Locate every Plasmodium falciparum-infected red blood cell.
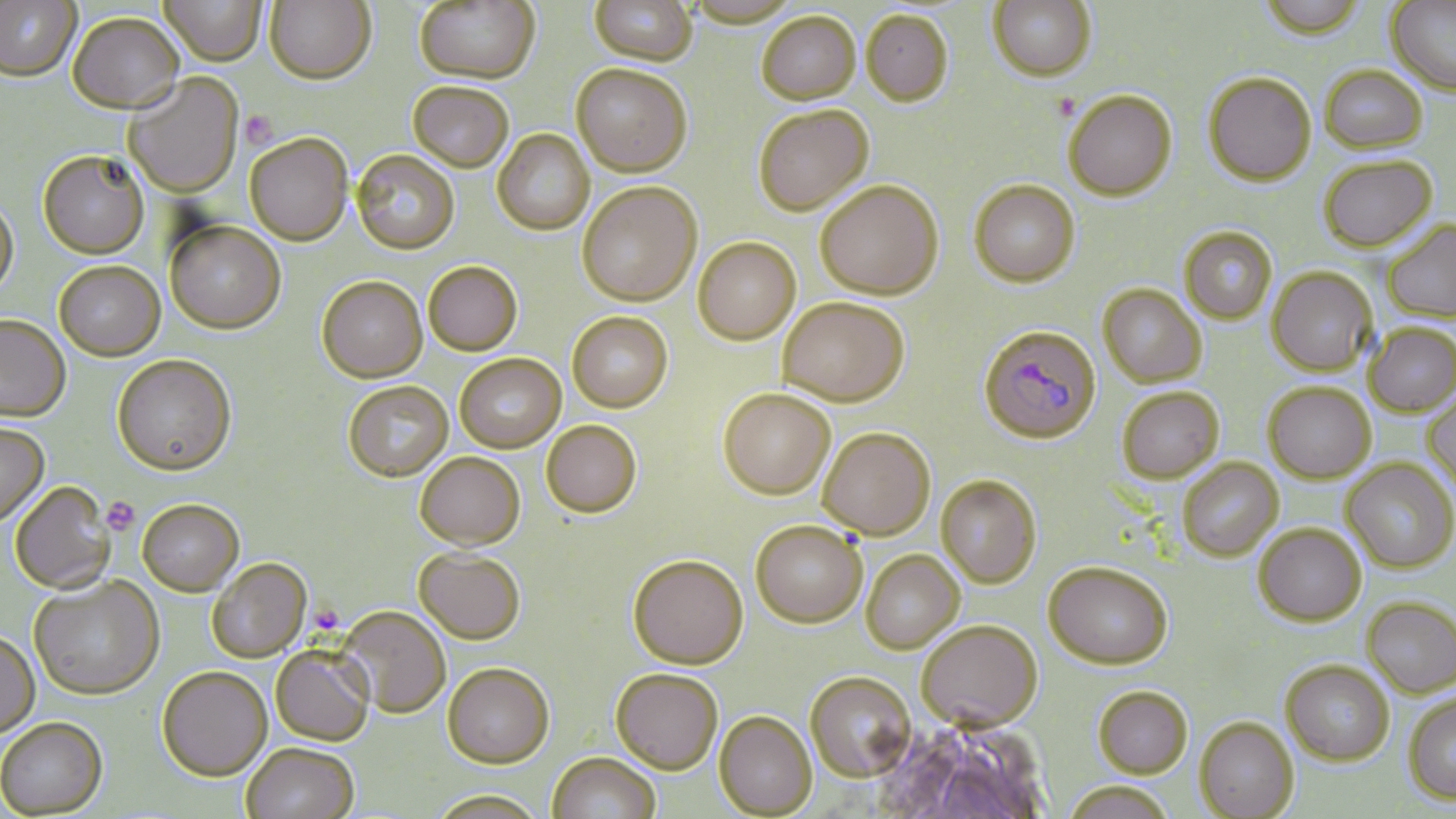
Approximate bounding boxes as named x1/y1/x2/y2 corners in pixels.
Plasmodium falciparum-infected red blood cells: (x1=979, y1=324, x2=1102, y2=444).

Summary:
  - Uninfected red blood cell locations: (x1=159, y1=0, x2=267, y2=66), (x1=265, y1=0, x2=376, y2=84), (x1=988, y1=0, x2=1096, y2=81), (x1=1256, y1=0, x2=1368, y2=41), (x1=0, y1=1, x2=81, y2=80), (x1=413, y1=1, x2=540, y2=83), (x1=590, y1=1, x2=698, y2=66), (x1=683, y1=1, x2=801, y2=28), (x1=1386, y1=1, x2=1456, y2=96), (x1=861, y1=9, x2=953, y2=106), (x1=67, y1=11, x2=184, y2=113), (x1=756, y1=11, x2=861, y2=104), (x1=571, y1=64, x2=692, y2=177), (x1=1320, y1=64, x2=1427, y2=153), (x1=1204, y1=71, x2=1316, y2=186), (x1=123, y1=72, x2=244, y2=198), (x1=408, y1=81, x2=514, y2=172), (x1=1063, y1=89, x2=1176, y2=200), (x1=752, y1=104, x2=874, y2=216), (x1=492, y1=129, x2=595, y2=235), (x1=245, y1=132, x2=353, y2=245), (x1=351, y1=149, x2=460, y2=254), (x1=38, y1=150, x2=149, y2=259), (x1=1319, y1=155, x2=1438, y2=252), (x1=969, y1=179, x2=1080, y2=286), (x1=815, y1=180, x2=943, y2=299), (x1=578, y1=182, x2=702, y2=306), (x1=0, y1=198, x2=19, y2=299), (x1=165, y1=220, x2=286, y2=334), (x1=1383, y1=220, x2=1456, y2=322), (x1=1179, y1=226, x2=1277, y2=324), (x1=693, y1=237, x2=801, y2=344), (x1=424, y1=260, x2=523, y2=355), (x1=54, y1=261, x2=165, y2=361), (x1=1267, y1=267, x2=1377, y2=377), (x1=317, y1=275, x2=427, y2=382), (x1=1098, y1=283, x2=1207, y2=387), (x1=778, y1=296, x2=909, y2=406), (x1=567, y1=311, x2=673, y2=412), (x1=0, y1=315, x2=71, y2=421), (x1=1364, y1=322, x2=1455, y2=417), (x1=455, y1=353, x2=566, y2=452), (x1=112, y1=354, x2=237, y2=476), (x1=343, y1=380, x2=453, y2=481), (x1=1263, y1=382, x2=1376, y2=484), (x1=1117, y1=386, x2=1224, y2=483), (x1=718, y1=388, x2=836, y2=499), (x1=1422, y1=388, x2=1456, y2=495), (x1=541, y1=419, x2=642, y2=517), (x1=0, y1=423, x2=49, y2=526), (x1=818, y1=427, x2=936, y2=540), (x1=415, y1=452, x2=525, y2=549), (x1=1178, y1=457, x2=1283, y2=561), (x1=1342, y1=458, x2=1456, y2=573), (x1=936, y1=474, x2=1042, y2=588), (x1=8, y1=482, x2=116, y2=595), (x1=137, y1=498, x2=244, y2=596), (x1=750, y1=520, x2=867, y2=627), (x1=1254, y1=523, x2=1366, y2=625), (x1=414, y1=547, x2=526, y2=643), (x1=861, y1=549, x2=964, y2=653), (x1=627, y1=554, x2=748, y2=669), (x1=207, y1=558, x2=311, y2=662), (x1=1043, y1=561, x2=1172, y2=669), (x1=29, y1=575, x2=165, y2=700), (x1=1362, y1=596, x2=1456, y2=697), (x1=339, y1=606, x2=451, y2=719), (x1=915, y1=619, x2=1042, y2=731), (x1=0, y1=631, x2=40, y2=738), (x1=270, y1=646, x2=375, y2=746), (x1=1281, y1=659, x2=1394, y2=765), (x1=443, y1=662, x2=554, y2=767), (x1=156, y1=665, x2=272, y2=780), (x1=610, y1=668, x2=723, y2=774), (x1=805, y1=671, x2=916, y2=780), (x1=1093, y1=685, x2=1193, y2=777), (x1=1402, y1=692, x2=1456, y2=804), (x1=715, y1=710, x2=817, y2=817), (x1=1194, y1=716, x2=1299, y2=818), (x1=0, y1=718, x2=108, y2=818), (x1=240, y1=743, x2=359, y2=819), (x1=546, y1=752, x2=661, y2=819), (x1=1062, y1=780, x2=1177, y2=819), (x1=425, y1=789, x2=550, y2=818)
  - Platelet locations: (x1=240, y1=111, x2=278, y2=148), (x1=101, y1=496, x2=141, y2=535)
  - Slide-level diagnosis: Plasmodium falciparum
  - Stain: May-Grünwald-Giemsa
  - Magnification: 1000x
  - Image size: 1456×819 pixels
  - Field of view: one of a larger specimen
  - Modality: light microscopy
  - Preparation: thin blood film